Point out each malaria parasite.
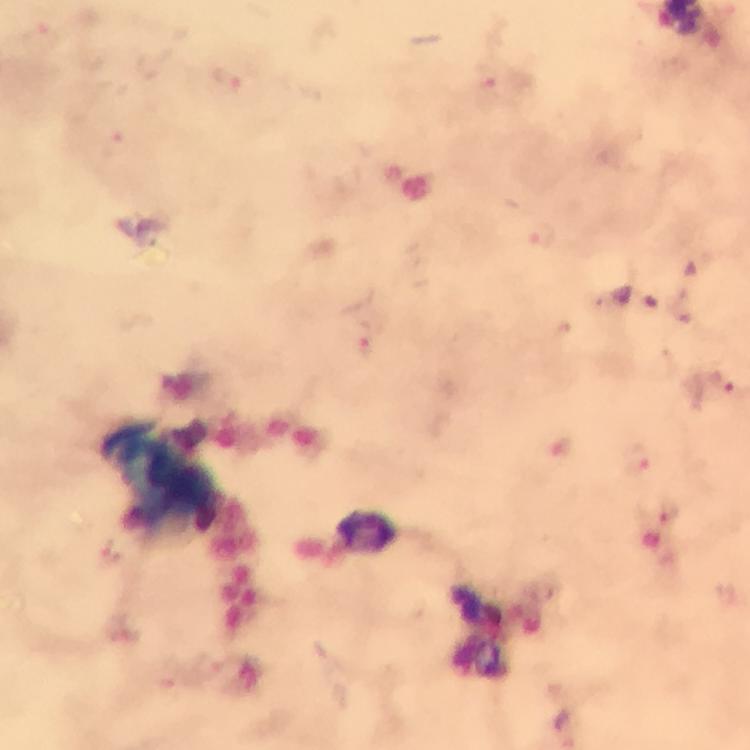

Approximate centers as [x, y] in pixels.
Malaria parasites: [226, 78], [486, 88], [544, 239], [368, 335], [725, 388], [636, 460], [666, 512].

Thick blood film. Cropped region of a single field of view. Smartphone photograph taken through a microscope. From a malaria diagnostic workup. Immersion oil was used. Image is 750×750 pixels. 100x magnification. Giemsa stain.